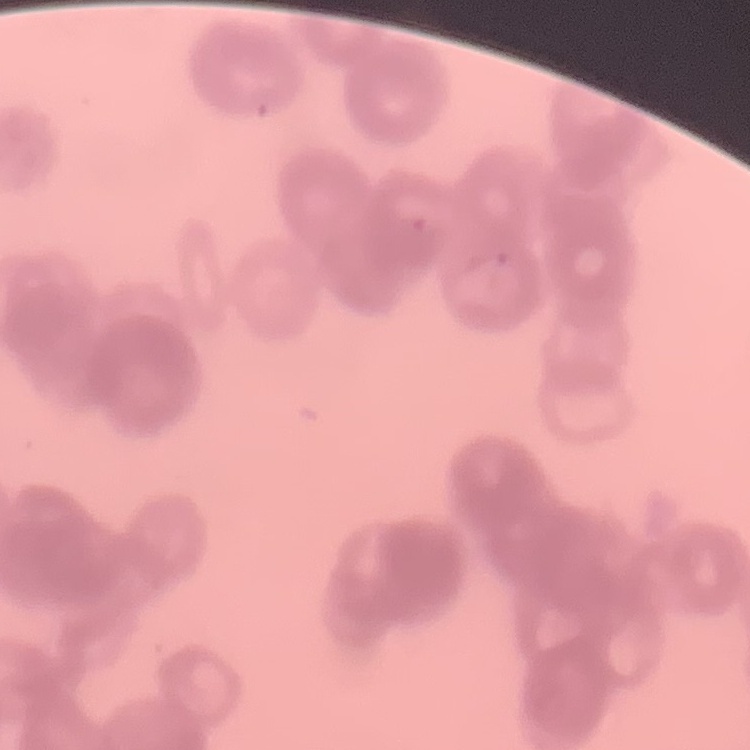

{
  "red_blood_cell_morphology": "rouleaux formation",
  "stain": "Field's or Giemsa",
  "preparation": "thin blood film",
  "image_type": "square crop of a larger photomicrograph"
}